Report the malaria status of this cell.
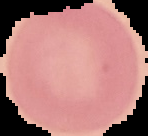

Uninfected.

image_type: segmented cell region with the area outside set to black
preparation: thin blood film
image_size: 148×136 pixels